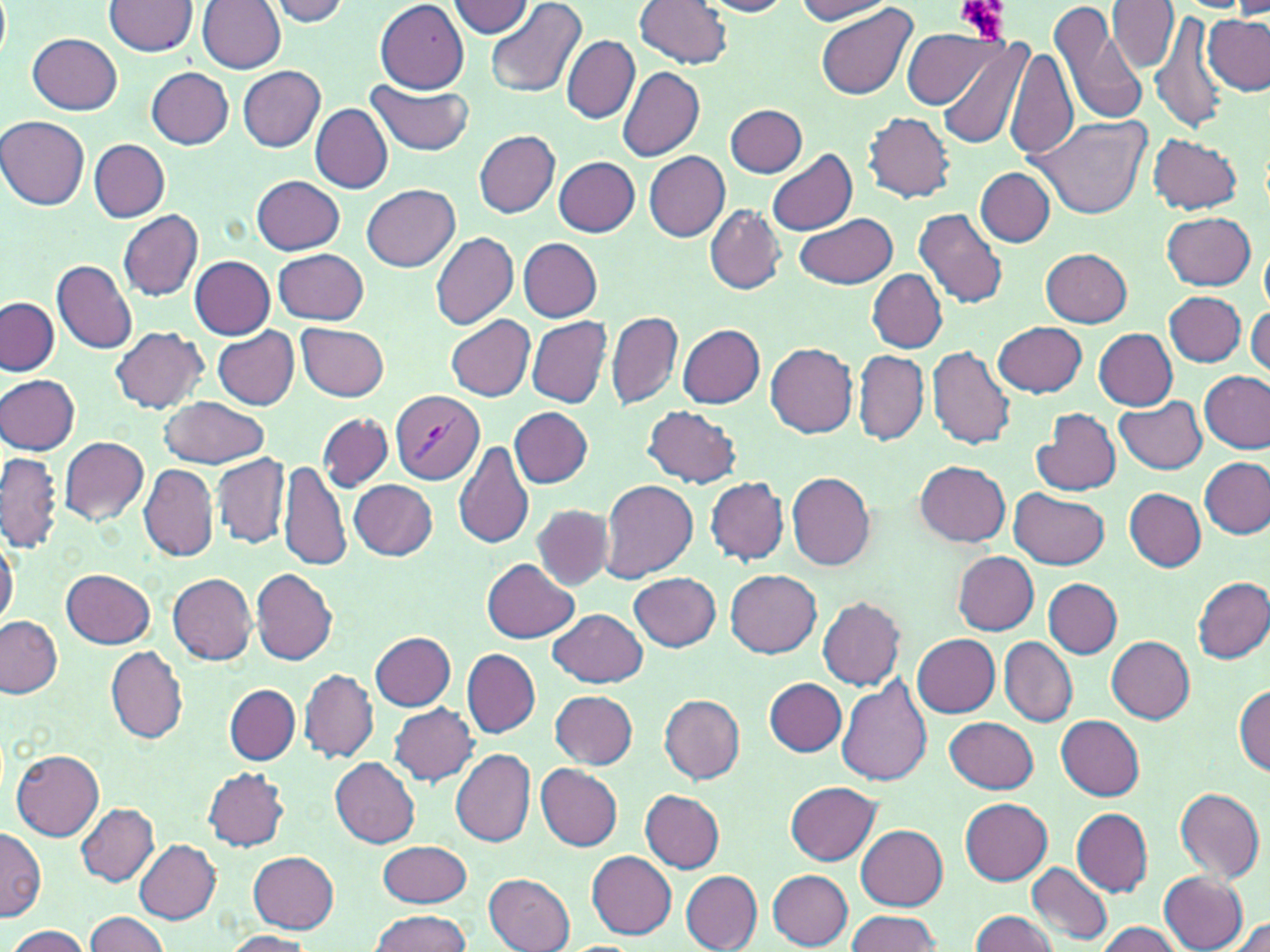

slide-level diagnosis = Plasmodium vivax
field of view = one of a larger specimen
modality = optical microscopy
preparation = thin blood film
magnification = 1000x
image size = 1270×952 pixels
stain = May-Grünwald-Giemsa
Plasmodium vivax-infected red blood cell locations = approximate bounding boxes as named x1/y1/x2/y2 corners in pixels: (x1=390, y1=390, x2=484, y2=485)
platelet locations = approximate bounding boxes as named x1/y1/x2/y2 corners in pixels: (x1=957, y1=0, x2=1010, y2=42)
uninfected red blood cell locations = approximate bounding boxes as named x1/y1/x2/y2 corners in pixels: (x1=198, y1=0, x2=287, y2=73), (x1=267, y1=0, x2=351, y2=26), (x1=485, y1=0, x2=588, y2=98), (x1=635, y1=0, x2=732, y2=68), (x1=794, y1=0, x2=894, y2=24), (x1=105, y1=1, x2=198, y2=55), (x1=448, y1=1, x2=532, y2=36), (x1=701, y1=1, x2=792, y2=17), (x1=1109, y1=1, x2=1179, y2=73), (x1=375, y1=2, x2=471, y2=92), (x1=1051, y1=2, x2=1149, y2=128), (x1=1233, y1=3, x2=1270, y2=19), (x1=816, y1=5, x2=915, y2=102), (x1=1151, y1=8, x2=1229, y2=133), (x1=1203, y1=15, x2=1269, y2=94), (x1=902, y1=26, x2=999, y2=108), (x1=28, y1=33, x2=122, y2=114), (x1=934, y1=33, x2=1032, y2=149), (x1=561, y1=34, x2=639, y2=122), (x1=1006, y1=44, x2=1077, y2=162), (x1=242, y1=64, x2=329, y2=240), (x1=238, y1=66, x2=324, y2=151), (x1=618, y1=66, x2=704, y2=163), (x1=146, y1=67, x2=235, y2=148), (x1=365, y1=78, x2=476, y2=156), (x1=725, y1=103, x2=808, y2=178), (x1=311, y1=105, x2=393, y2=194), (x1=864, y1=112, x2=956, y2=202), (x1=1030, y1=112, x2=1150, y2=219), (x1=1, y1=117, x2=92, y2=210), (x1=473, y1=129, x2=560, y2=218), (x1=1149, y1=133, x2=1241, y2=214), (x1=90, y1=139, x2=169, y2=222), (x1=767, y1=149, x2=857, y2=236), (x1=645, y1=152, x2=730, y2=241), (x1=554, y1=156, x2=640, y2=237), (x1=977, y1=167, x2=1053, y2=247), (x1=251, y1=175, x2=346, y2=254), (x1=360, y1=183, x2=459, y2=271), (x1=705, y1=206, x2=784, y2=294), (x1=914, y1=208, x2=1008, y2=310), (x1=119, y1=210, x2=203, y2=301), (x1=797, y1=211, x2=897, y2=289), (x1=1162, y1=211, x2=1257, y2=291), (x1=429, y1=231, x2=518, y2=329), (x1=518, y1=238, x2=603, y2=321), (x1=1260, y1=241, x2=1270, y2=317), (x1=274, y1=248, x2=369, y2=324), (x1=1041, y1=249, x2=1133, y2=326), (x1=189, y1=255, x2=274, y2=338), (x1=52, y1=259, x2=136, y2=353), (x1=868, y1=269, x2=947, y2=352), (x1=1164, y1=291, x2=1246, y2=366), (x1=1, y1=297, x2=59, y2=376), (x1=1246, y1=305, x2=1269, y2=380), (x1=607, y1=311, x2=682, y2=410), (x1=444, y1=314, x2=535, y2=401), (x1=526, y1=316, x2=612, y2=407), (x1=296, y1=321, x2=390, y2=401), (x1=994, y1=321, x2=1087, y2=397), (x1=677, y1=323, x2=765, y2=408), (x1=110, y1=326, x2=209, y2=415), (x1=214, y1=326, x2=300, y2=410), (x1=1094, y1=329, x2=1177, y2=410), (x1=765, y1=343, x2=859, y2=437), (x1=927, y1=345, x2=1016, y2=450), (x1=853, y1=350, x2=928, y2=446), (x1=1200, y1=370, x2=1269, y2=453), (x1=1, y1=374, x2=81, y2=454), (x1=159, y1=397, x2=271, y2=469), (x1=1116, y1=397, x2=1208, y2=474), (x1=509, y1=407, x2=592, y2=488), (x1=643, y1=407, x2=741, y2=486), (x1=1033, y1=408, x2=1121, y2=497), (x1=316, y1=412, x2=393, y2=493), (x1=57, y1=436, x2=149, y2=525), (x1=455, y1=440, x2=534, y2=549), (x1=1, y1=452, x2=63, y2=552), (x1=211, y1=452, x2=290, y2=549), (x1=1200, y1=457, x2=1268, y2=538), (x1=279, y1=460, x2=349, y2=572), (x1=917, y1=461, x2=1011, y2=546), (x1=140, y1=464, x2=218, y2=563), (x1=786, y1=470, x2=875, y2=571), (x1=706, y1=476, x2=788, y2=565), (x1=599, y1=479, x2=698, y2=581), (x1=349, y1=480, x2=437, y2=560), (x1=1125, y1=488, x2=1206, y2=572), (x1=1010, y1=489, x2=1110, y2=569), (x1=533, y1=505, x2=614, y2=589), (x1=0, y1=533, x2=19, y2=628), (x1=953, y1=552, x2=1039, y2=635), (x1=482, y1=557, x2=579, y2=642), (x1=250, y1=566, x2=337, y2=666), (x1=61, y1=567, x2=155, y2=648), (x1=725, y1=569, x2=820, y2=656), (x1=629, y1=571, x2=721, y2=650), (x1=167, y1=572, x2=256, y2=665), (x1=1194, y1=577, x2=1269, y2=663), (x1=1044, y1=579, x2=1123, y2=657), (x1=817, y1=596, x2=906, y2=690), (x1=549, y1=607, x2=647, y2=686), (x1=0, y1=616, x2=64, y2=699), (x1=371, y1=631, x2=456, y2=710), (x1=913, y1=633, x2=1000, y2=718), (x1=1105, y1=635, x2=1195, y2=723), (x1=998, y1=637, x2=1076, y2=727), (x1=107, y1=646, x2=188, y2=743), (x1=463, y1=648, x2=540, y2=737), (x1=298, y1=669, x2=378, y2=762), (x1=836, y1=675, x2=934, y2=787), (x1=764, y1=677, x2=846, y2=757), (x1=225, y1=684, x2=300, y2=765), (x1=1234, y1=684, x2=1269, y2=775), (x1=550, y1=690, x2=638, y2=768), (x1=659, y1=694, x2=746, y2=784), (x1=389, y1=701, x2=478, y2=785), (x1=1057, y1=715, x2=1145, y2=800), (x1=944, y1=716, x2=1039, y2=794), (x1=10, y1=748, x2=105, y2=840), (x1=451, y1=749, x2=535, y2=846), (x1=331, y1=757, x2=420, y2=847), (x1=535, y1=762, x2=622, y2=851), (x1=202, y1=766, x2=289, y2=850), (x1=785, y1=780, x2=881, y2=864), (x1=1174, y1=787, x2=1265, y2=884), (x1=639, y1=789, x2=725, y2=872), (x1=960, y1=799, x2=1052, y2=883), (x1=76, y1=803, x2=159, y2=886), (x1=1072, y1=808, x2=1153, y2=895), (x1=856, y1=825, x2=947, y2=909), (x1=0, y1=827, x2=46, y2=922), (x1=135, y1=840, x2=220, y2=923), (x1=377, y1=840, x2=471, y2=906), (x1=248, y1=851, x2=338, y2=932), (x1=587, y1=851, x2=677, y2=939), (x1=1027, y1=862, x2=1112, y2=944), (x1=768, y1=868, x2=853, y2=949), (x1=680, y1=870, x2=764, y2=951), (x1=1159, y1=871, x2=1249, y2=951), (x1=484, y1=872, x2=576, y2=952), (x1=369, y1=909, x2=472, y2=952), (x1=846, y1=909, x2=942, y2=951), (x1=969, y1=910, x2=1059, y2=952), (x1=85, y1=911, x2=170, y2=952), (x1=1224, y1=917, x2=1270, y2=952), (x1=1094, y1=922, x2=1184, y2=952), (x1=5, y1=925, x2=92, y2=951), (x1=222, y1=930, x2=313, y2=952)